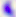

{
  "modality": "photomicrograph",
  "magnification": "400x",
  "identification": "Toxoplasma gondii"
}